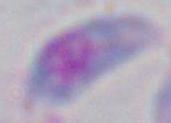
Summary:
  - Modality: photomicrograph
  - Magnification: 1000x
  - Identification: Toxoplasma gondii